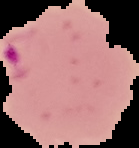

Image is 139×148 pixels. Result: Plasmodium parasites detected. The area outside the segmented cell region is set to black. From a thin blood film.